Give the extent of all uninfected red blood cells.
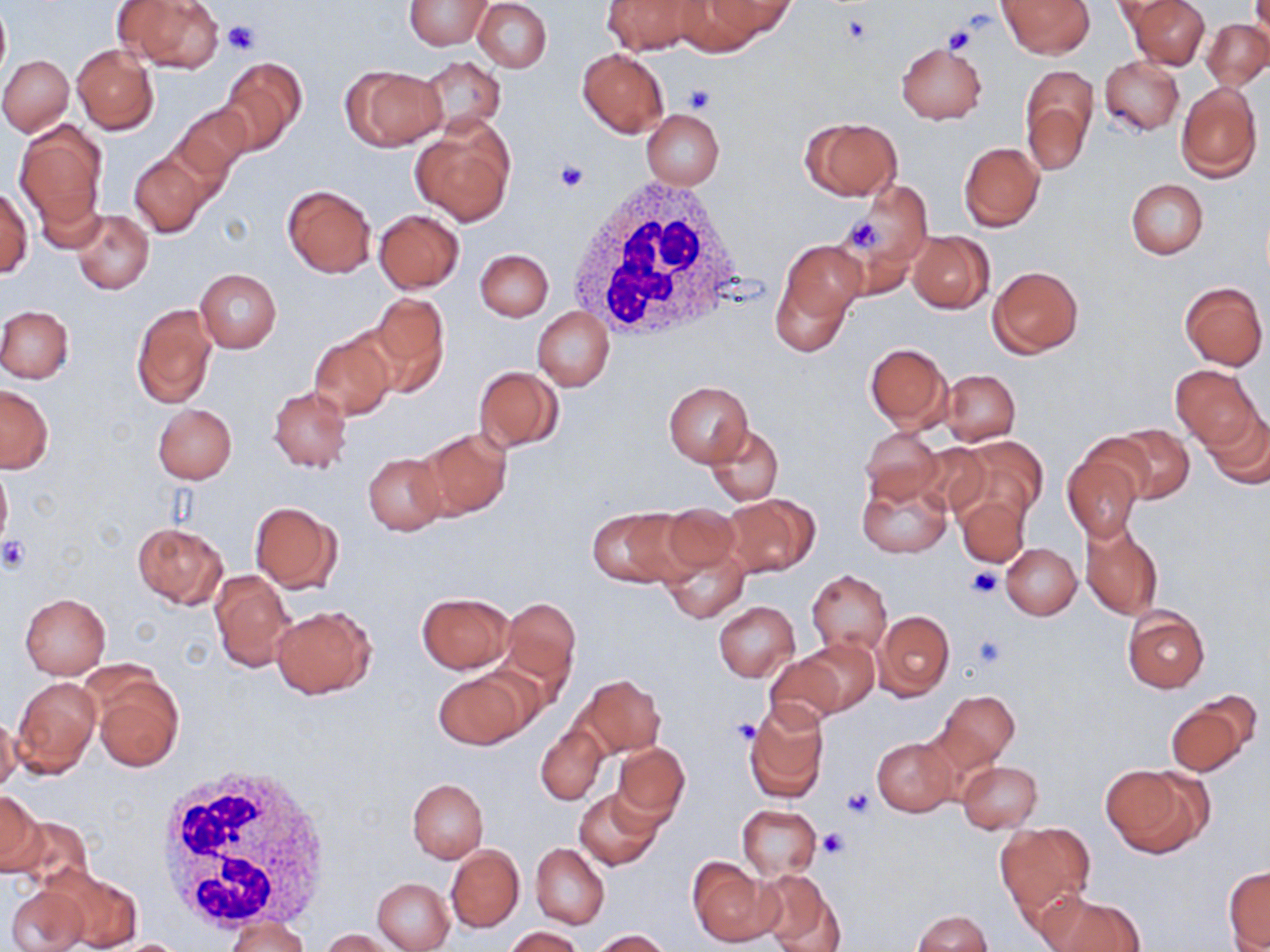
Approximate bounding boxes as [x1, y1, x2, y2] in pixels.
Uninfected red blood cells: [114, 0, 224, 72], [404, 0, 491, 49], [474, 0, 552, 73], [601, 0, 705, 55], [708, 0, 796, 38], [997, 0, 1093, 57], [1128, 0, 1209, 68], [671, 1, 770, 54], [0, 4, 10, 86], [1203, 20, 1270, 90], [896, 42, 988, 123], [72, 44, 159, 135], [577, 49, 670, 138], [0, 54, 74, 137], [414, 56, 506, 137], [1099, 56, 1185, 136], [219, 57, 306, 152], [342, 64, 445, 151], [1020, 67, 1098, 175], [1176, 83, 1262, 182], [172, 103, 252, 186], [642, 109, 724, 189], [801, 118, 901, 200], [411, 120, 515, 226], [14, 123, 108, 233], [959, 142, 1044, 231], [129, 152, 210, 237], [1126, 179, 1208, 258], [280, 183, 376, 278], [839, 186, 932, 280], [0, 187, 32, 278], [71, 209, 154, 294], [374, 210, 464, 292], [908, 231, 994, 313], [772, 242, 864, 352], [475, 249, 553, 321], [989, 266, 1083, 357], [195, 269, 282, 353], [1178, 282, 1268, 370], [364, 294, 450, 395], [130, 303, 218, 409], [0, 306, 74, 382], [533, 307, 613, 390], [309, 329, 398, 420], [865, 342, 952, 429], [1170, 364, 1263, 450], [473, 367, 564, 451], [940, 370, 1020, 446], [664, 380, 754, 467], [1, 386, 53, 473], [268, 386, 352, 474], [153, 404, 236, 483], [1200, 407, 1270, 489], [705, 424, 782, 506], [1112, 424, 1194, 503], [860, 426, 942, 505], [413, 427, 512, 521], [955, 436, 1047, 526], [915, 441, 993, 516], [1061, 448, 1145, 541], [363, 453, 447, 536], [0, 462, 12, 553], [857, 471, 952, 558], [954, 493, 1030, 567], [721, 494, 819, 578], [249, 500, 342, 595], [660, 503, 745, 579], [588, 505, 696, 589], [132, 522, 228, 609], [1081, 522, 1162, 620], [1, 527, 27, 576], [659, 539, 750, 624], [1001, 543, 1081, 620], [210, 570, 295, 672], [806, 570, 891, 655], [416, 592, 514, 674], [19, 593, 110, 680], [498, 598, 581, 692], [714, 602, 799, 681], [271, 605, 375, 699], [1121, 607, 1208, 693], [874, 610, 953, 699], [796, 639, 879, 714], [763, 652, 847, 730], [433, 670, 531, 750], [576, 673, 665, 758], [89, 676, 183, 773], [11, 677, 101, 778], [935, 689, 1021, 770], [1166, 695, 1258, 776], [742, 702, 829, 804], [0, 714, 21, 795], [535, 723, 608, 805], [872, 735, 959, 817], [612, 741, 690, 826], [956, 760, 1043, 832], [1101, 764, 1209, 857], [406, 778, 488, 862], [574, 786, 663, 870], [0, 790, 45, 876], [737, 804, 822, 880], [12, 815, 96, 895], [995, 823, 1096, 916], [530, 843, 609, 929], [446, 846, 523, 931], [687, 856, 780, 947], [1224, 866, 1269, 951], [757, 867, 846, 952], [51, 869, 142, 950], [372, 877, 455, 951], [6, 883, 90, 952], [1041, 891, 1144, 952], [913, 910, 993, 952], [225, 917, 309, 952], [504, 926, 585, 952], [321, 929, 393, 951], [589, 929, 671, 951], [110, 938, 194, 951].

White blood cell locations: [568, 175, 755, 346], [157, 760, 335, 935]. Platelet locations: [840, 13, 875, 46], [222, 22, 258, 55], [942, 25, 976, 54], [682, 83, 718, 114], [555, 160, 590, 193], [841, 212, 889, 255], [0, 535, 31, 572], [966, 567, 1002, 599], [972, 634, 1006, 668], [732, 719, 761, 747], [840, 787, 875, 820], [818, 829, 849, 858]. Slide-level diagnosis: negative for blood parasites. Light microscopy. May-Grünwald-Giemsa-stained preparation. Thin blood smear. Image is 1270×952 pixels. 1000x magnification. Single field of view.